Assess this cell for malaria.
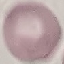

It is uninfected.

Summary:
  - Stain: Giemsa
  - Image type: cell patch, automatically extracted from a larger field of view and resized to 64 × 64 pixels
  - Preparation: thin smear
  - Capture: smartphone through the microscope eyepiece